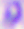
identification: Toxoplasma gondii
magnification: 400x
modality: photomicrograph